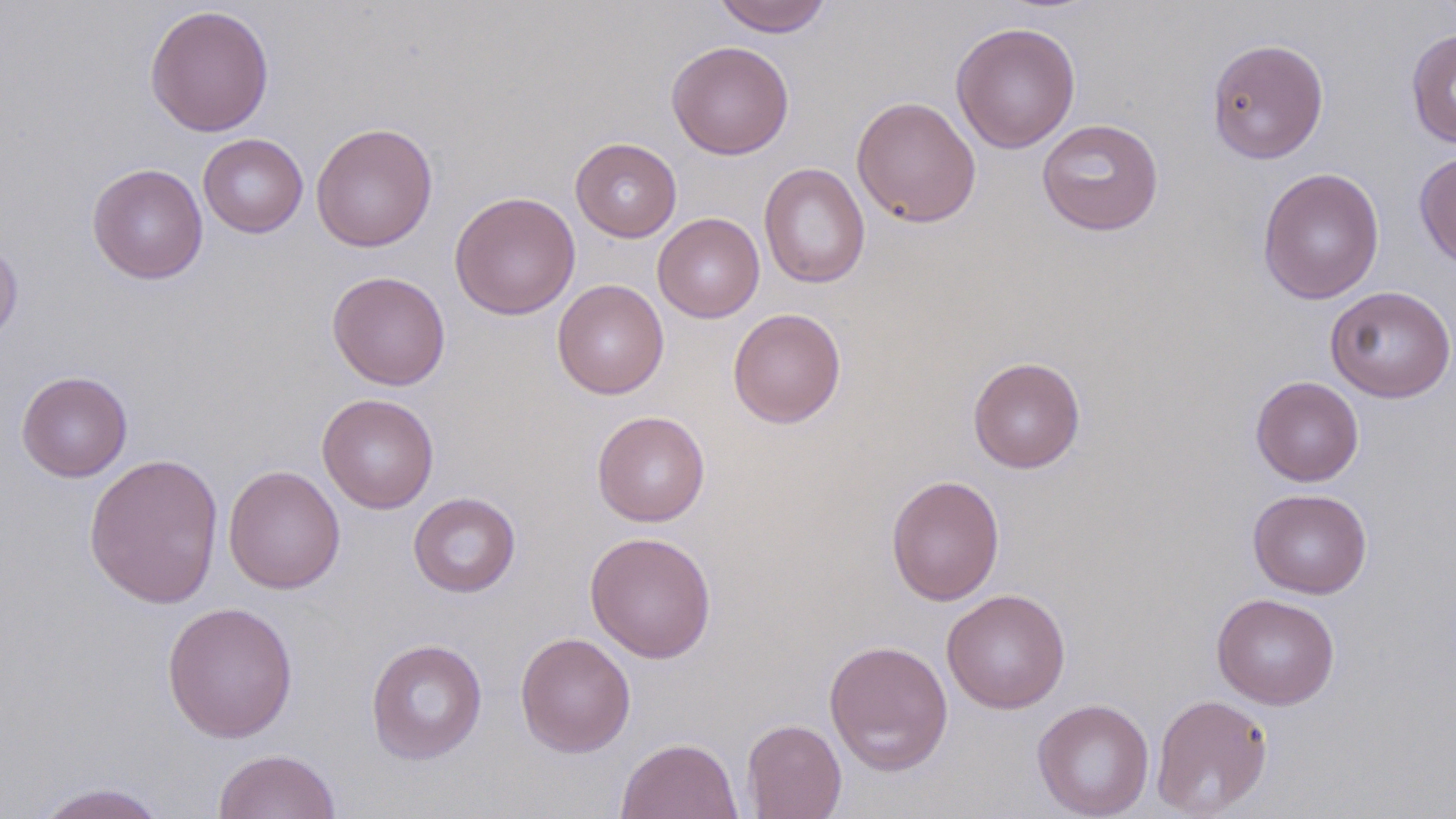 Approximate bounding boxes as (x1,y1)-(x2,y2) corner pairs in pixels. Uninfected red blood cell locations: (712,0)-(833,37), (144,4)-(274,137), (951,21)-(1081,153), (1406,28)-(1456,149), (1206,38)-(1329,164), (666,41)-(794,160), (851,96)-(981,228), (1037,118)-(1164,236), (311,122)-(437,252), (198,133)-(308,238), (571,137)-(682,242), (1414,150)-(1456,270), (758,162)-(871,288), (87,163)-(208,285), (1257,166)-(1385,305), (449,191)-(580,320), (652,213)-(765,323), (0,239)-(23,348), (327,270)-(451,390), (552,278)-(669,399), (1325,285)-(1456,402), (728,307)-(846,428), (968,356)-(1085,473), (16,370)-(132,481), (1250,376)-(1364,486), (317,394)-(439,513), (592,411)-(710,526), (84,452)-(224,610), (223,465)-(345,594), (886,474)-(1004,606), (1248,488)-(1372,599), (408,492)-(521,597), (585,531)-(717,662), (942,588)-(1071,714), (1211,592)-(1340,709), (161,600)-(299,743), (515,631)-(636,757), (365,638)-(488,765), (823,638)-(954,775), (1151,693)-(1273,817), (1032,698)-(1154,818), (742,718)-(847,818), (615,736)-(743,819), (212,748)-(341,819), (31,782)-(169,819). Slide-level diagnosis: no evidence of blood parasites. Image is 1456×819 pixels. Light microscopy. Single field of view. Captured at 1000x magnification. May-Grünwald-Giemsa stain. Thin blood smear.